Comment on the morphology of the red blood cells.
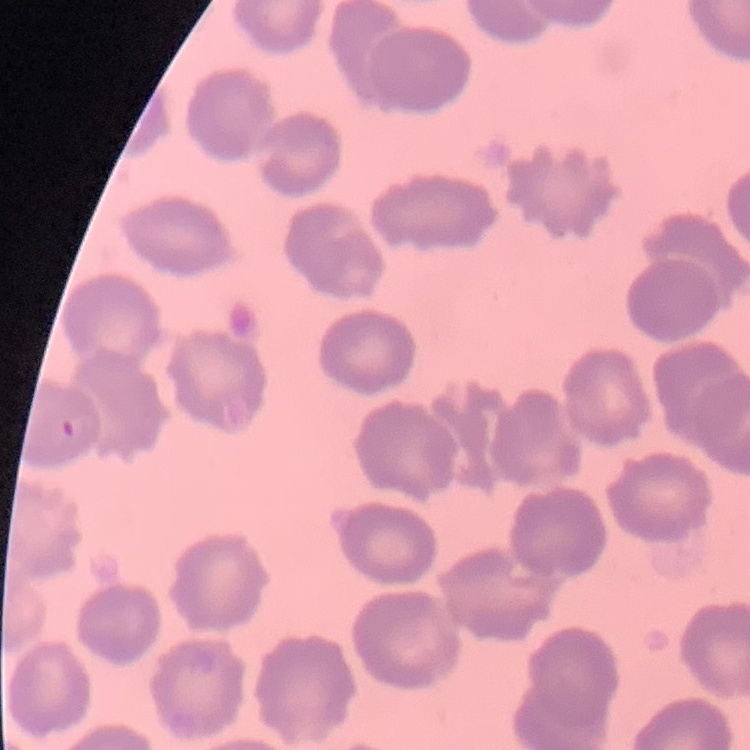

They show no rouleaux formation.

Thin blood smear. One tile cut from a larger photomicrograph. Field's or Giemsa stain.